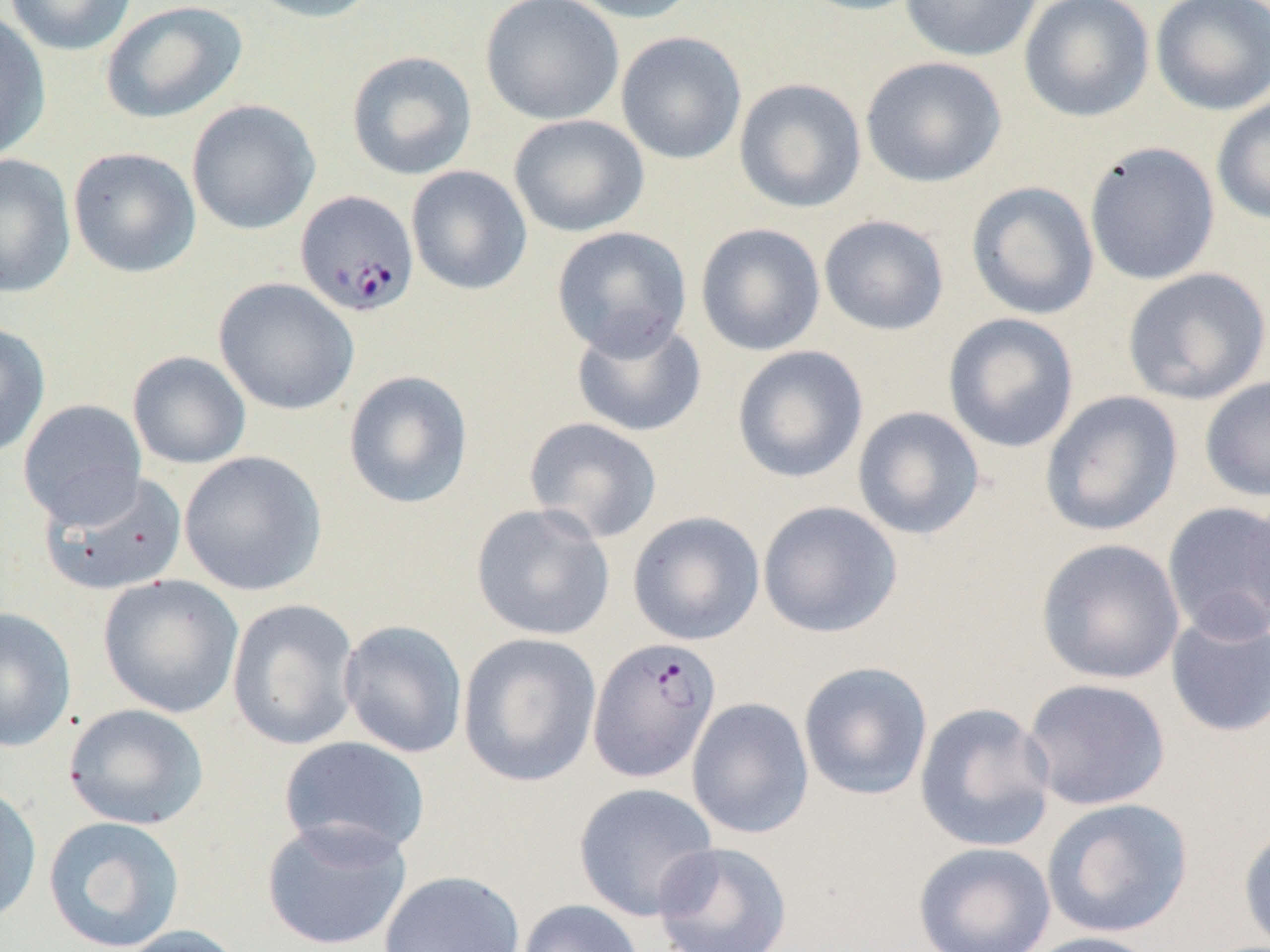

Summary:
  - Coordinate format: approximate bounding boxes as (x1,y1)-(x2,y2) corner pairs in pixels
  - Plasmodium falciparum-infected red blood cell locations: (295,190)-(419,318), (587,636)-(722,783)
  - Uninfected red blood cell locations: (4,0)-(137,56), (244,0)-(383,23), (479,0)-(625,126), (563,0)-(702,24), (790,0)-(929,17), (900,0)-(1043,62), (1019,0)-(1155,123), (1150,0)-(1270,116), (100,1)-(247,124), (0,12)-(51,162), (615,32)-(747,165), (346,50)-(477,181), (860,56)-(1007,188), (733,78)-(867,213), (1211,94)-(1270,225), (186,99)-(320,235), (508,114)-(650,238), (1084,141)-(1220,285), (67,147)-(201,279), (0,153)-(77,298), (406,166)-(533,295), (966,181)-(1099,320), (818,214)-(950,336), (695,222)-(826,356), (552,225)-(692,358), (1122,267)-(1270,405), (213,277)-(359,416), (942,312)-(1080,453), (570,315)-(707,439), (0,322)-(51,459), (731,345)-(868,483), (127,351)-(251,469), (342,370)-(474,509), (1200,375)-(1270,503), (1039,390)-(1183,537), (18,399)-(147,527), (852,406)-(986,540), (523,416)-(663,544), (178,450)-(327,596), (39,470)-(188,596), (1244,491)-(1270,629), (757,500)-(903,638), (1162,501)-(1270,642), (470,502)-(616,641), (627,511)-(765,646), (1035,537)-(1185,685), (97,574)-(244,719), (227,598)-(361,751), (0,607)-(77,753), (1165,610)-(1270,738), (338,619)-(468,758), (457,632)-(603,787), (798,661)-(934,801), (1021,677)-(1171,811), (686,697)-(814,840), (914,702)-(1056,852), (63,703)-(209,830), (279,735)-(431,861), (0,782)-(42,926), (572,782)-(720,922), (1042,797)-(1194,938), (43,815)-(185,951), (261,818)-(413,951), (1238,823)-(1270,951), (652,841)-(793,952), (913,841)-(1056,952), (379,869)-(525,952), (516,899)-(646,952), (113,924)-(248,952), (1018,930)-(1163,952)
  - Slide-level diagnosis: Plasmodium falciparum
  - Preparation: thin blood smear
  - Modality: light microscopy
  - Field of view: one of a larger specimen
  - Image size: 1270×952 pixels
  - Magnification: 1000x